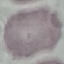 Malaria status: uninfected. Automatically extracted cell patch, resized to 64 × 64 pixels. Acquired by smartphone through the microscope eyepiece. Giemsa-stained preparation. Thin smear of blood.